Report the malaria status of this cell.
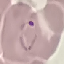
It is parasitized.

Thin blood smear. Automatically extracted cell patch, resized to 64 × 64 pixels. Photographed with a smartphone camera at the microscope eyepiece. Giemsa-stained preparation.